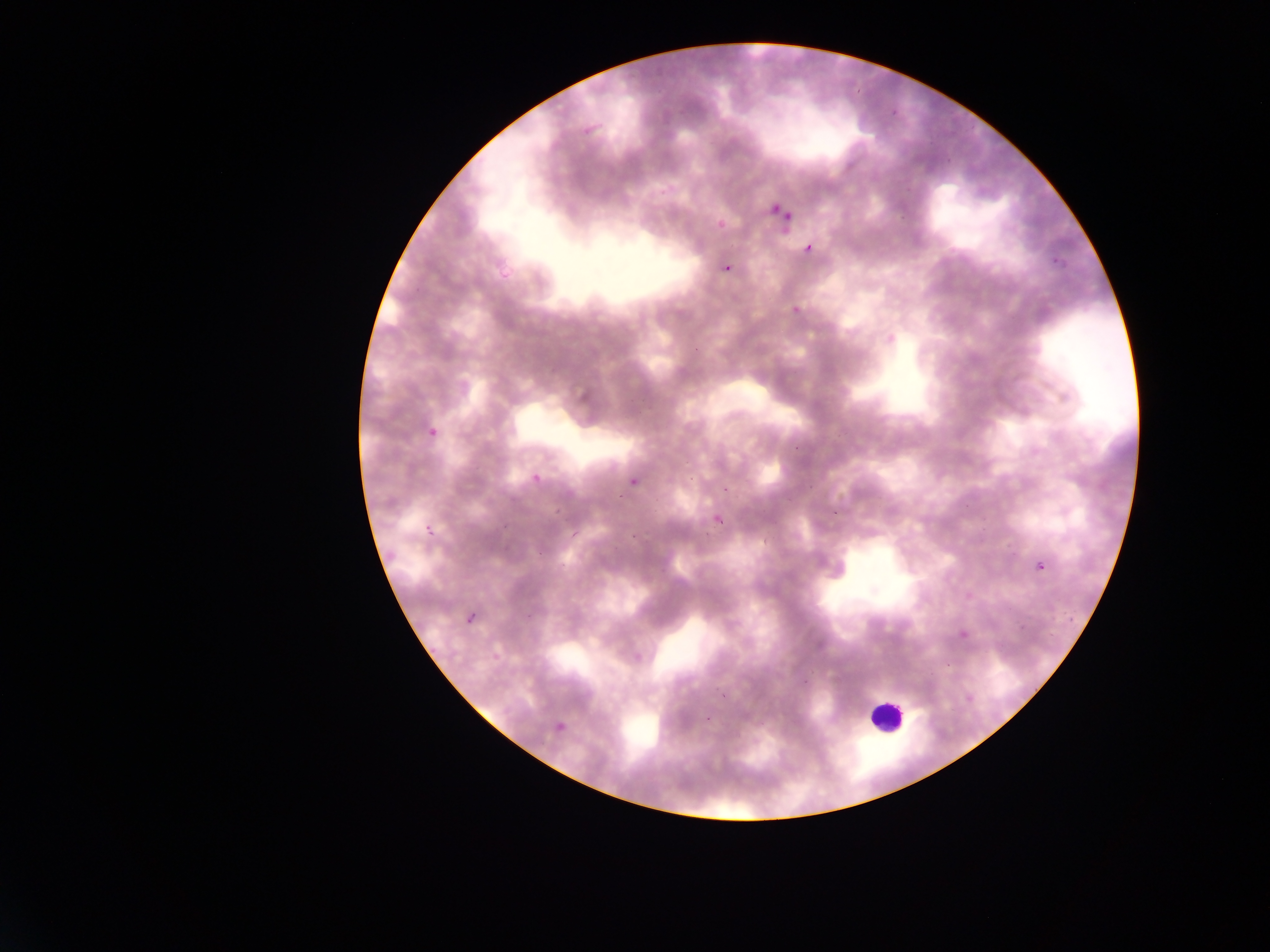
Approximate bounding boxes as {left, top, right, bottom} in pixels. Plasmodium parasite locations: {771, 204, 780, 213}, {784, 212, 792, 221}, {803, 244, 812, 254}, {711, 255, 742, 281}, {407, 416, 453, 444}, {625, 458, 648, 493}, {528, 468, 545, 493}, {494, 483, 522, 508}, {706, 493, 736, 529}, {418, 514, 448, 537}, {1034, 557, 1050, 574}, {466, 613, 476, 625}, {490, 652, 499, 661}, {546, 711, 582, 736}. Leukocyte locations: {869, 695, 907, 741}. One field of view. Image is 1270×952 pixels. Thin blood smear. Photographed through a microscope with a mobile-phone camera. Collected in Ghana.